Classify this cell by malaria status.
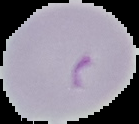

It is parasitized.

image size = 139×124 pixels
image type = segmented cell region with the area outside set to black
preparation = thin blood film